Report the malaria status of this cell.
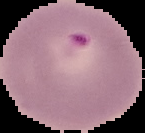

Parasitized.

Summary:
  - Preparation: thin blood film
  - Image size: 145×133 pixels
  - Image type: segmented cell region with the area outside set to black